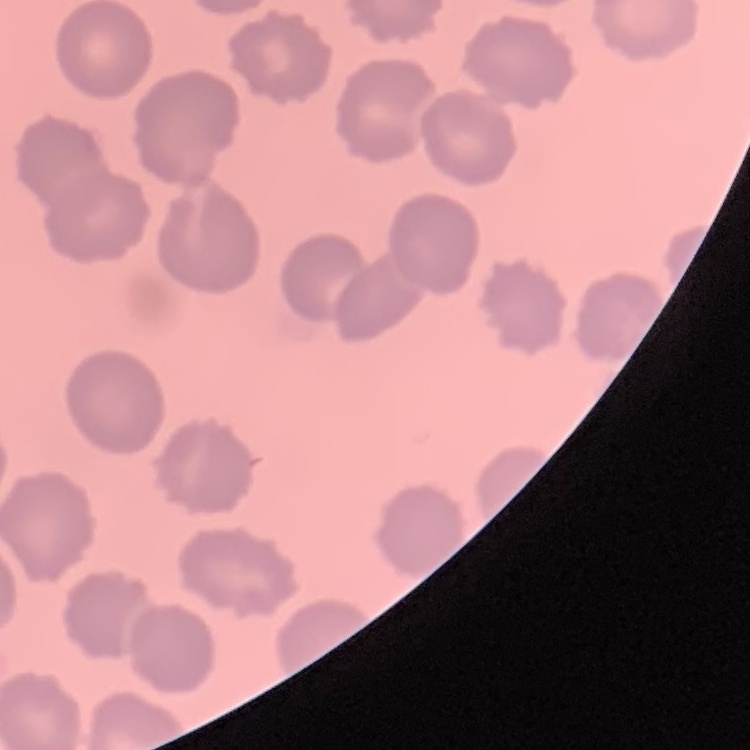 The erythrocytes show no rouleaux formation. Thin blood film. Stained with either Field's or Giemsa. One tile cut from a larger photomicrograph.